Assess this cell for malaria.
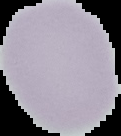

Uninfected.

Summary:
  - Image type: cell region segmented out of the field of view; surrounding area masked to black
  - Image size: 121×136 pixels
  - Preparation: thin blood film